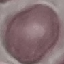
result = no malaria parasites seen
preparation = thin blood smear
stain = Giemsa
image type = cell patch, automatically extracted from a larger field of view and resized to 64 × 64 pixels
capture = smartphone camera at the microscope eyepiece